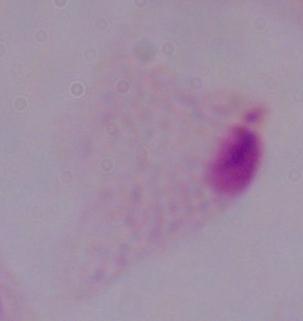
Captured at 1000x magnification. A trichomonad is shown. Photomicrograph.